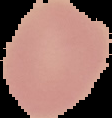
Summary:
  - Image type: segmented cell region with the area outside set to black
  - Image size: 112×118 pixels
  - Preparation: thin blood smear
  - Malaria status: uninfected